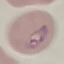
Summary:
  - Malaria status: parasitized
  - Capture: smartphone through the microscope eyepiece
  - Image type: automatically extracted cell patch, resized to 64 × 64 pixels
  - Stain: Giemsa
  - Preparation: thin smear